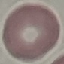

Summary:
  - Result: no malaria parasites seen
  - Preparation: thin blood smear
  - Image type: cell patch, automatically extracted from a larger field of view and resized to 64 × 64 pixels
  - Capture: smartphone camera at the microscope eyepiece
  - Stain: Giemsa